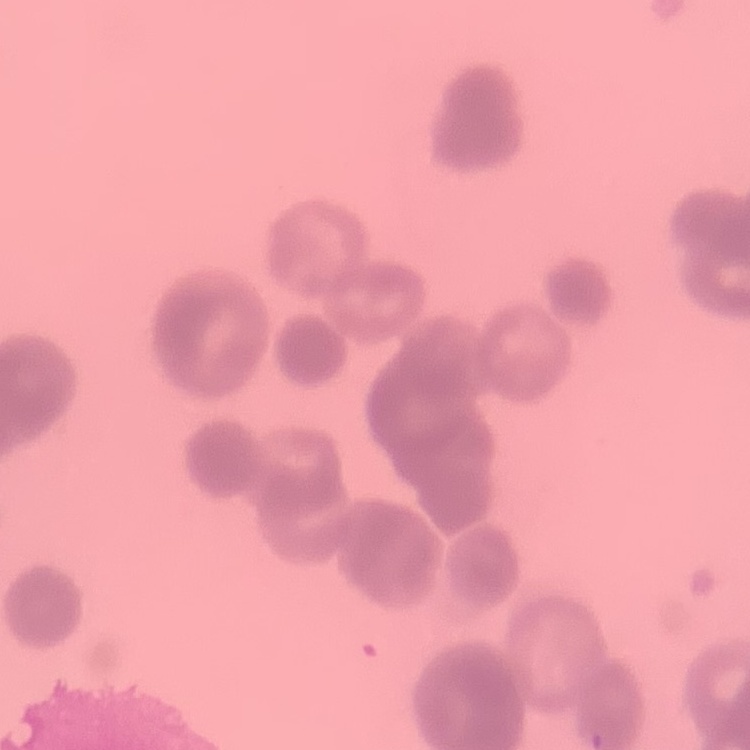 The red blood cells show rouleaux formation. Field's or Giemsa stain. Square crop of a larger photomicrograph. Thin peripheral smear.